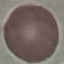 Malaria status: uninfected. Photographed with a smartphone camera at the microscope eyepiece. Cell patch, automatically extracted from a larger field of view and resized to 64 × 64 pixels. Thin smear of blood. Giemsa stain.